Assess the morphology of the red blood cells.
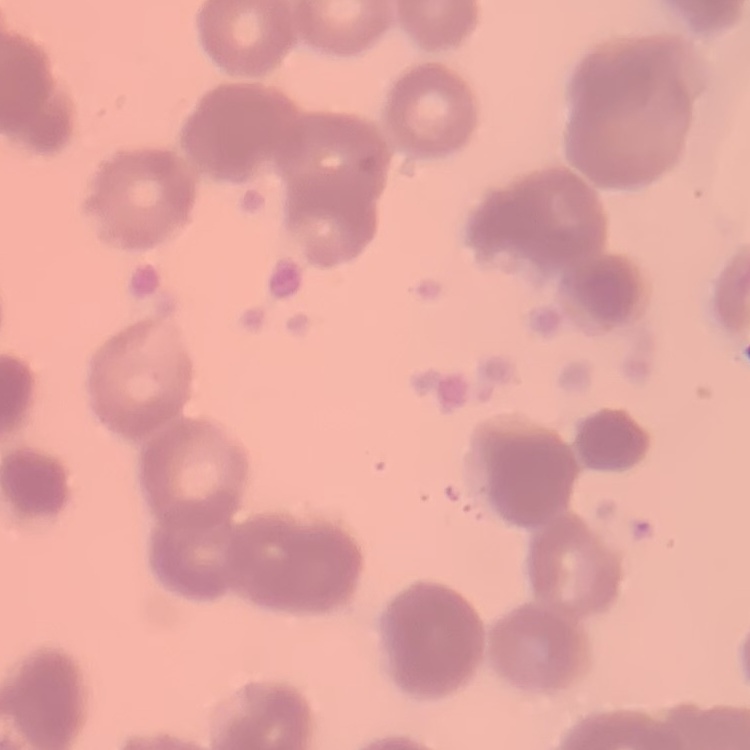
Rouleaux formation.

Summary:
  - Image type: square crop of a larger photomicrograph
  - Stain: Field's or Giemsa
  - Preparation: thin blood film